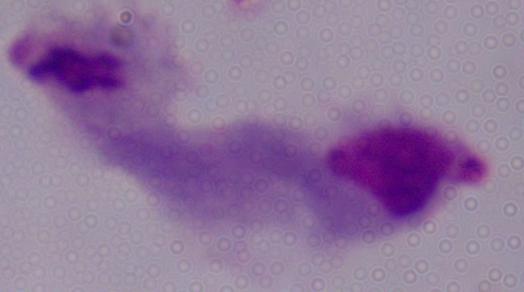

Summary:
  - Modality: photomicrograph
  - Identification: trichomonad
  - Magnification: 1000x